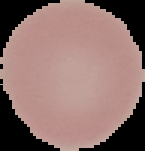
Image is 145×151 pixels. Malaria status: uninfected. Segmented cell region on a black background. From a thin blood film.